Comment on the morphology of the erythrocytes.
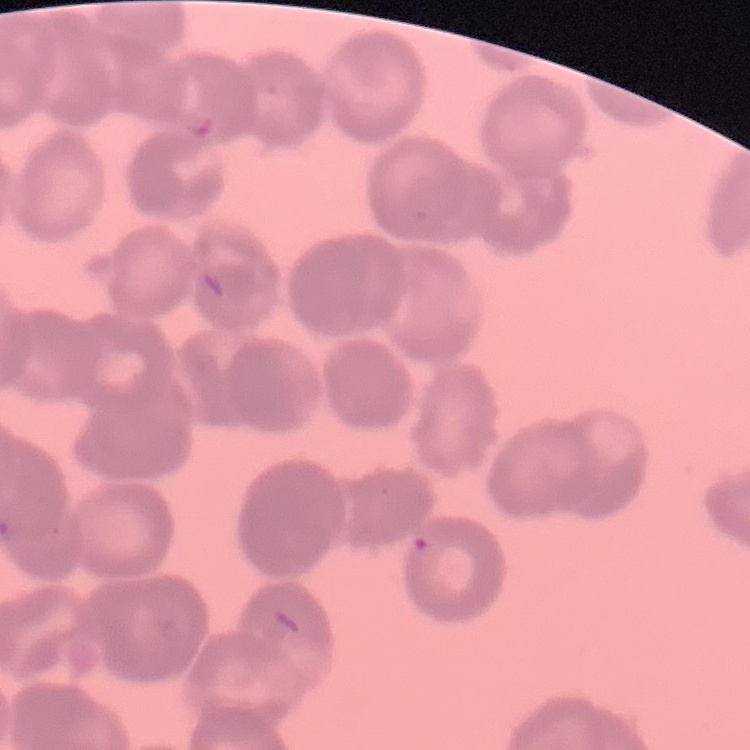
Rouleaux formation.

Summary:
  - Preparation: thin blood smear
  - Image type: square crop of a larger photomicrograph
  - Stain: Field's or Giemsa